Name the parasite shown.
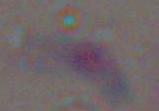

This is Toxoplasma gondii.

Summary:
  - Magnification: 1000x
  - Modality: photomicrograph